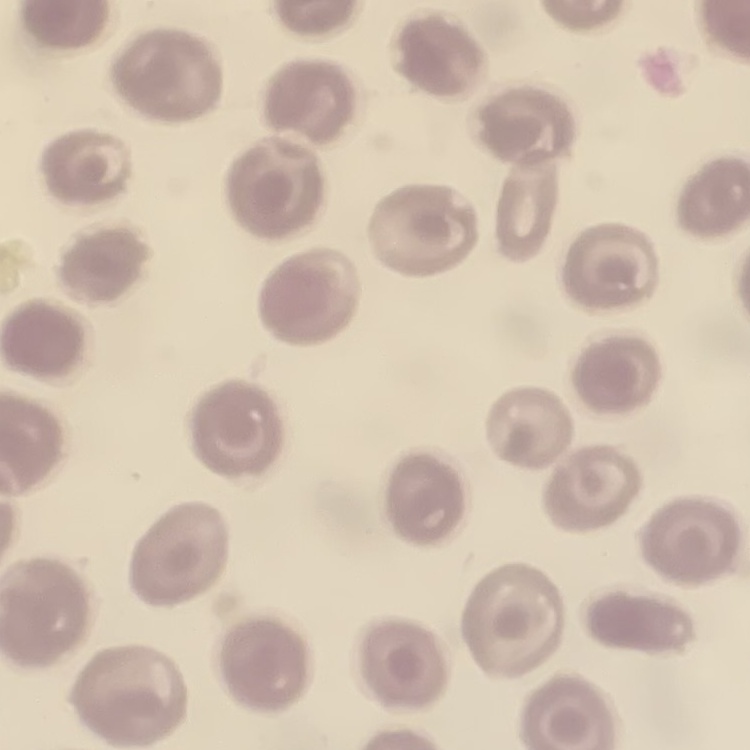

Summary:
  - Red blood cell morphology: no rouleaux formation
  - Image type: one tile cut from a larger photomicrograph
  - Preparation: thin blood smear
  - Stain: Field's or Giemsa